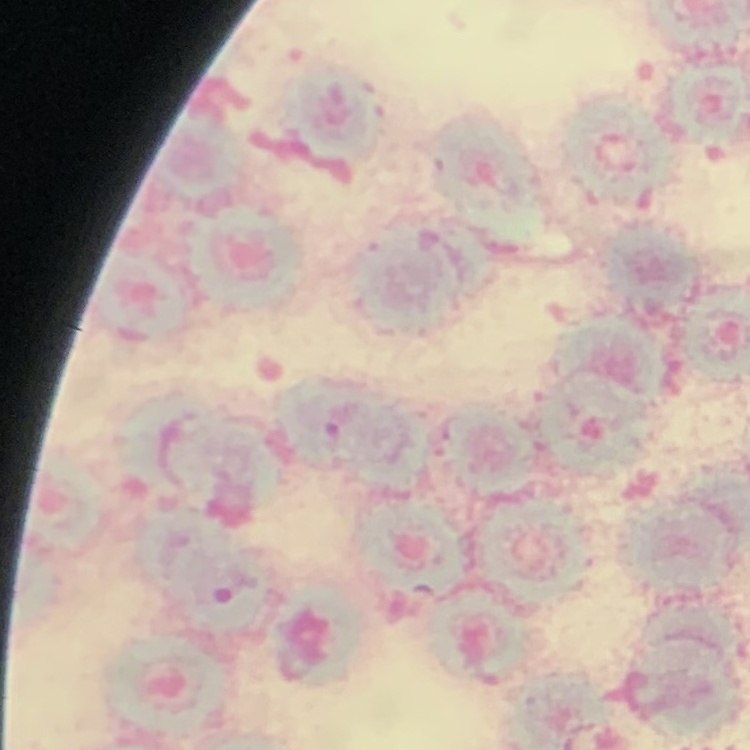 The erythrocytes exhibit rouleaux formation. Square crop of a larger photomicrograph. Stained with either Field's or Giemsa. Thin peripheral smear.